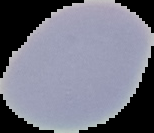
{
  "image_size": "154×133 pixels",
  "malaria_status": "uninfected",
  "image_type": "segmented cell region on a black background",
  "preparation": "thin blood smear"
}